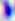 Photomicrograph. 400x magnification. Toxoplasma gondii is shown.